Assess this cell for malaria.
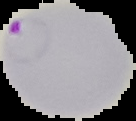
Parasitized.

Summary:
  - Preparation: thin blood smear
  - Image size: 136×121 pixels
  - Image type: cell region segmented out of the field of view; surrounding area masked to black